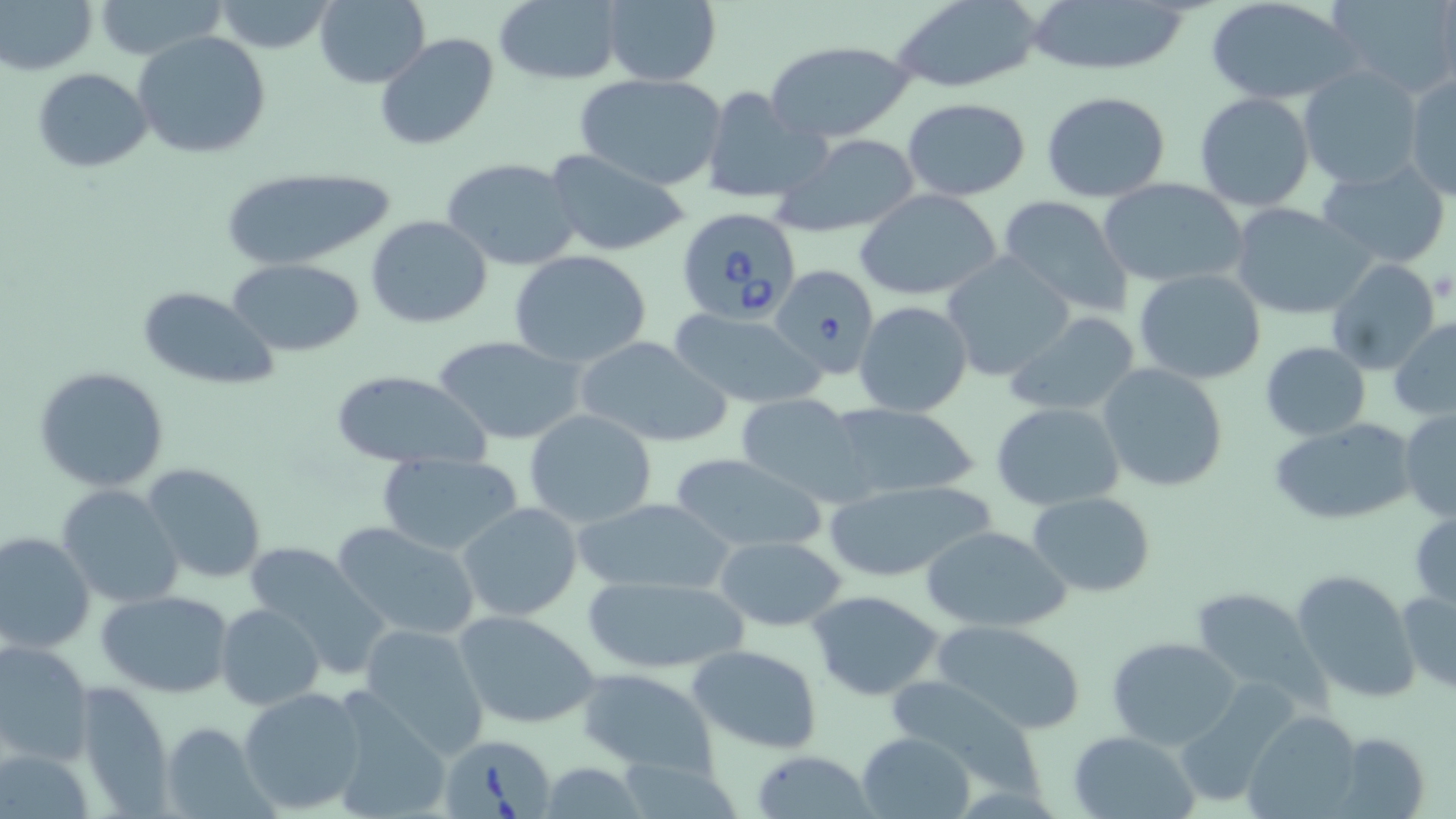 Approximate bounding boxes as [x1, y1, x2, y2] in pixels. Uninfected red blood cell locations: [1, 0, 97, 76], [92, 0, 228, 60], [211, 0, 340, 54], [315, 0, 431, 89], [1205, 0, 1360, 106], [1329, 0, 1456, 97], [493, 1, 622, 85], [891, 1, 1045, 93], [1024, 1, 1196, 76], [601, 2, 721, 85], [135, 31, 272, 160], [374, 33, 499, 152], [763, 38, 919, 143], [1299, 66, 1425, 190], [32, 67, 151, 171], [1404, 70, 1455, 199], [574, 73, 728, 191], [698, 86, 829, 206], [1042, 92, 1170, 203], [1194, 93, 1315, 211], [901, 98, 1030, 200], [774, 133, 924, 239], [543, 148, 695, 257], [441, 156, 582, 270], [1316, 164, 1453, 269], [222, 168, 388, 271], [1100, 179, 1249, 289], [855, 190, 1003, 301], [996, 195, 1135, 317], [1228, 202, 1375, 321], [365, 215, 493, 329], [508, 251, 655, 369], [942, 254, 1074, 380], [228, 258, 366, 355], [1327, 259, 1441, 374], [1134, 269, 1265, 384], [136, 286, 278, 389], [854, 301, 972, 418], [668, 307, 827, 410], [1005, 310, 1144, 418], [1390, 318, 1456, 418], [433, 335, 590, 446], [573, 335, 733, 450], [1259, 341, 1371, 441], [1097, 364, 1229, 493], [32, 366, 169, 492], [329, 369, 493, 472], [732, 394, 868, 500], [991, 401, 1126, 512], [821, 403, 983, 504], [1400, 409, 1455, 523], [524, 410, 657, 527], [1268, 419, 1419, 526], [376, 453, 524, 557], [670, 453, 830, 556], [142, 463, 267, 584], [824, 477, 998, 583], [56, 483, 186, 608], [1028, 492, 1156, 596], [573, 495, 734, 596], [458, 502, 582, 621], [1409, 508, 1456, 609], [331, 520, 483, 643], [923, 525, 1071, 632], [0, 530, 96, 654], [714, 535, 848, 632], [242, 543, 391, 678], [1292, 569, 1420, 703], [575, 573, 755, 673], [1398, 587, 1456, 694], [1189, 588, 1324, 705], [98, 589, 234, 698], [805, 590, 944, 700], [215, 603, 324, 711], [452, 610, 600, 730], [930, 619, 1084, 735], [358, 623, 492, 761], [1106, 635, 1241, 749], [0, 638, 95, 766], [685, 644, 821, 756], [573, 668, 721, 777], [886, 673, 1045, 801], [71, 680, 175, 815], [239, 686, 368, 814], [326, 695, 450, 819], [1242, 710, 1361, 817], [159, 723, 270, 817], [857, 730, 975, 818], [1069, 731, 1201, 819], [1337, 731, 1430, 818], [2, 744, 96, 817], [751, 750, 874, 818], [537, 761, 649, 817]. Babesia divergens-infected red blood cell locations: [674, 206, 800, 326], [769, 264, 878, 381], [442, 736, 557, 819]. Slide-level diagnosis: Babesia divergens. Light microscopy. May-Grünwald-Giemsa stain. 1000x magnification. One field of a larger specimen. Image is 1456×819 pixels. Thin blood film.